Outline each blood parasite and name the species.
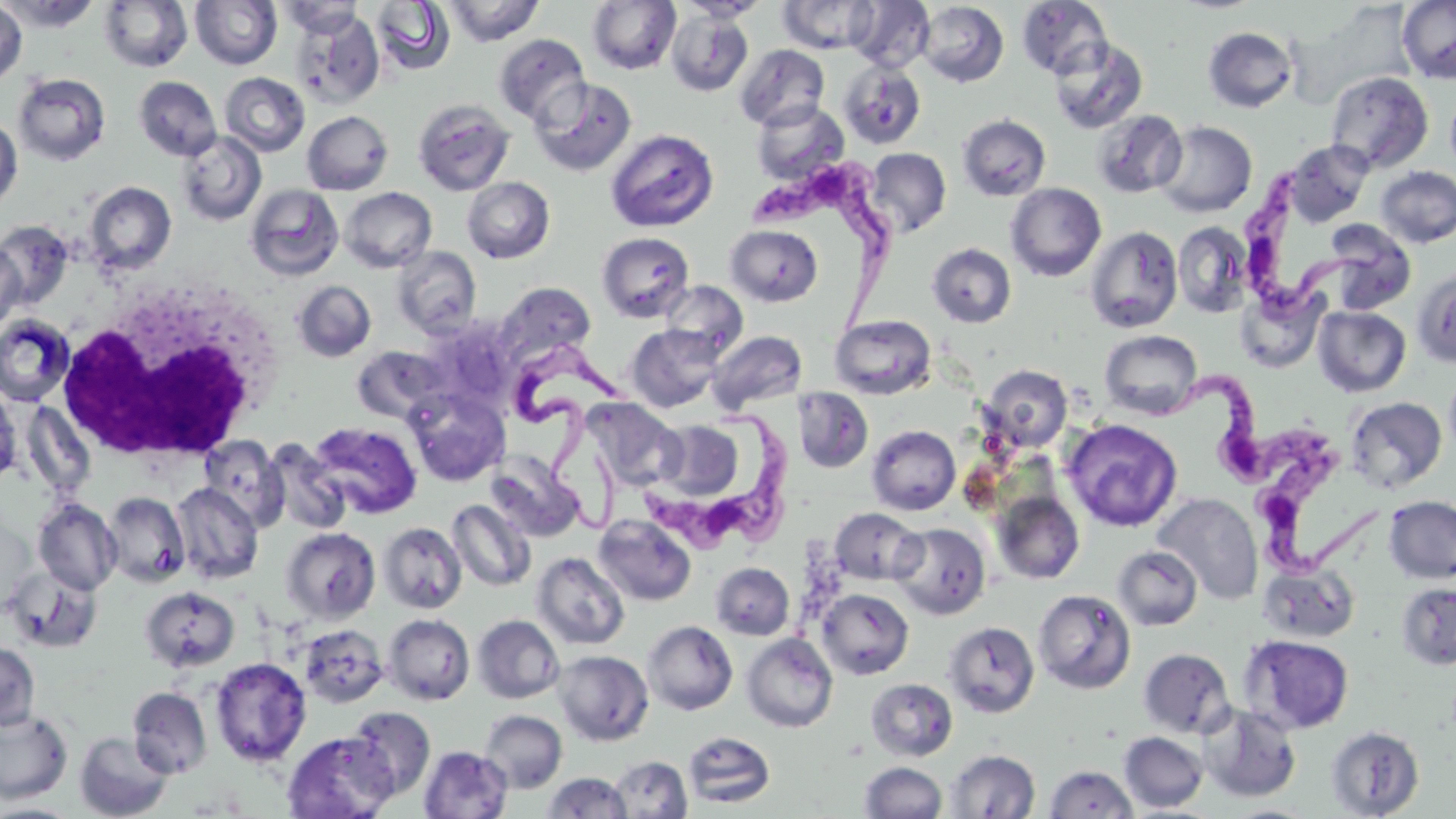

Approximate bounding boxes as (x1,y1)-(x2,y2) corner pairs in pixels.
Trypanosoma brucei: (744,155)-(902,340), (1223,160)-(1400,320), (516,330)-(630,546), (1141,379)-(1330,478), (639,399)-(799,564), (1255,447)-(1402,588).
No Plasmodium falciparum, Plasmodium ovale, Plasmodium malariae, Plasmodium vivax, or Babesia divergens observed.

Summary:
  - Uninfected red blood cell locations: (2,0)-(102,31), (440,0)-(545,46), (587,0)-(681,74), (677,0)-(770,22), (846,0)-(935,73), (1017,0)-(1113,79), (1397,0)-(1456,85), (0,1)-(28,87), (98,1)-(193,73), (190,1)-(282,70), (278,1)-(364,38), (371,1)-(456,76), (777,1)-(880,54), (916,1)-(1008,87), (290,9)-(385,109), (665,9)-(753,96), (1203,27)-(1297,112), (494,34)-(590,126), (1049,37)-(1148,134), (735,44)-(830,130), (838,63)-(927,150), (1325,70)-(1434,173), (220,72)-(310,156), (13,73)-(111,166), (134,76)-(222,160), (530,78)-(636,176), (1446,88)-(1456,179), (412,98)-(515,196), (751,101)-(848,184), (1092,109)-(1187,198), (302,110)-(394,195), (957,114)-(1051,201), (0,116)-(22,210), (1155,121)-(1257,218), (605,129)-(719,232), (176,130)-(267,226), (1283,139)-(1374,227), (866,147)-(951,237), (1375,166)-(1456,248), (461,177)-(555,264), (84,181)-(176,274), (245,183)-(345,281), (1006,183)-(1106,281), (340,187)-(437,272), (1,219)-(75,309), (1172,222)-(1253,318), (725,224)-(823,307), (1322,224)-(1416,314), (1085,226)-(1183,333), (596,232)-(695,323), (0,243)-(26,333), (927,243)-(1017,329), (391,246)-(481,338), (1413,267)-(1456,368), (292,280)-(376,362), (659,280)-(748,360), (495,281)-(596,366), (1235,285)-(1327,374), (1313,306)-(1411,397), (0,314)-(75,407), (830,315)-(936,399), (626,325)-(722,412), (708,329)-(805,414), (1099,330)-(1203,420), (351,345)-(452,424), (982,365)-(1073,452), (1444,367)-(1456,459), (404,386)-(511,486), (0,387)-(21,488), (792,387)-(873,473), (585,397)-(683,490), (1345,397)-(1447,494), (650,418)-(750,505), (1062,419)-(1182,532), (308,421)-(422,519), (867,425)-(961,515), (199,435)-(287,530), (263,439)-(351,535), (487,454)-(586,544), (171,483)-(264,584), (991,491)-(1086,584), (103,492)-(191,589), (1152,492)-(1264,604), (1384,496)-(1456,584), (33,499)-(121,595), (447,499)-(536,592), (830,507)-(924,586), (594,514)-(696,606), (378,522)-(466,614), (890,523)-(991,619), (280,527)-(381,624), (1113,546)-(1202,631), (532,552)-(630,650), (710,562)-(795,640), (1258,563)-(1359,642), (2,564)-(103,653), (1396,581)-(1456,670), (140,585)-(240,672), (817,588)-(914,680), (1033,589)-(1136,694), (382,613)-(475,705), (472,614)-(565,704), (642,621)-(738,715), (944,621)-(1040,718), (299,623)-(388,708), (741,633)-(838,732), (1242,635)-(1354,734), (0,642)-(40,729), (1139,648)-(1234,739), (553,650)-(654,746), (211,657)-(312,766), (865,678)-(958,762), (127,686)-(212,778), (1198,703)-(1302,802), (345,706)-(436,802), (0,708)-(72,803), (479,709)-(567,793), (1325,725)-(1424,818), (75,731)-(173,819), (283,731)-(397,819), (1120,731)-(1208,812), (683,732)-(775,809), (419,745)-(512,819), (945,749)-(1040,818), (609,755)-(692,817), (860,761)-(947,818), (1044,765)-(1138,817), (543,772)-(632,818), (0,802)-(81,817)
  - White blood cell locations: (55,291)-(277,463)
  - Slide-level diagnosis: Trypanosoma brucei
  - Modality: light microscopy
  - Image size: 1456×819 pixels
  - Field of view: single
  - Preparation: thin blood film
  - Magnification: 1000x
  - Stain: May-Grünwald-Giemsa